Report the malaria status of this cell.
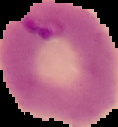

It is parasitized.

preparation = thin blood smear
image size = 118×127 pixels
image type = segmented cell region with the area outside set to black